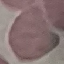

Summary:
  - Result: no malaria parasites seen
  - Image type: cell patch, automatically extracted from a larger field of view and resized to 64 × 64 pixels
  - Stain: Giemsa
  - Preparation: thin smear
  - Capture: smartphone through the microscope eyepiece